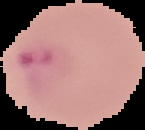

Summary:
  - Image size: 145×130 pixels
  - Malaria status: parasitized
  - Image type: segmented cell region on a black background
  - Preparation: thin blood smear